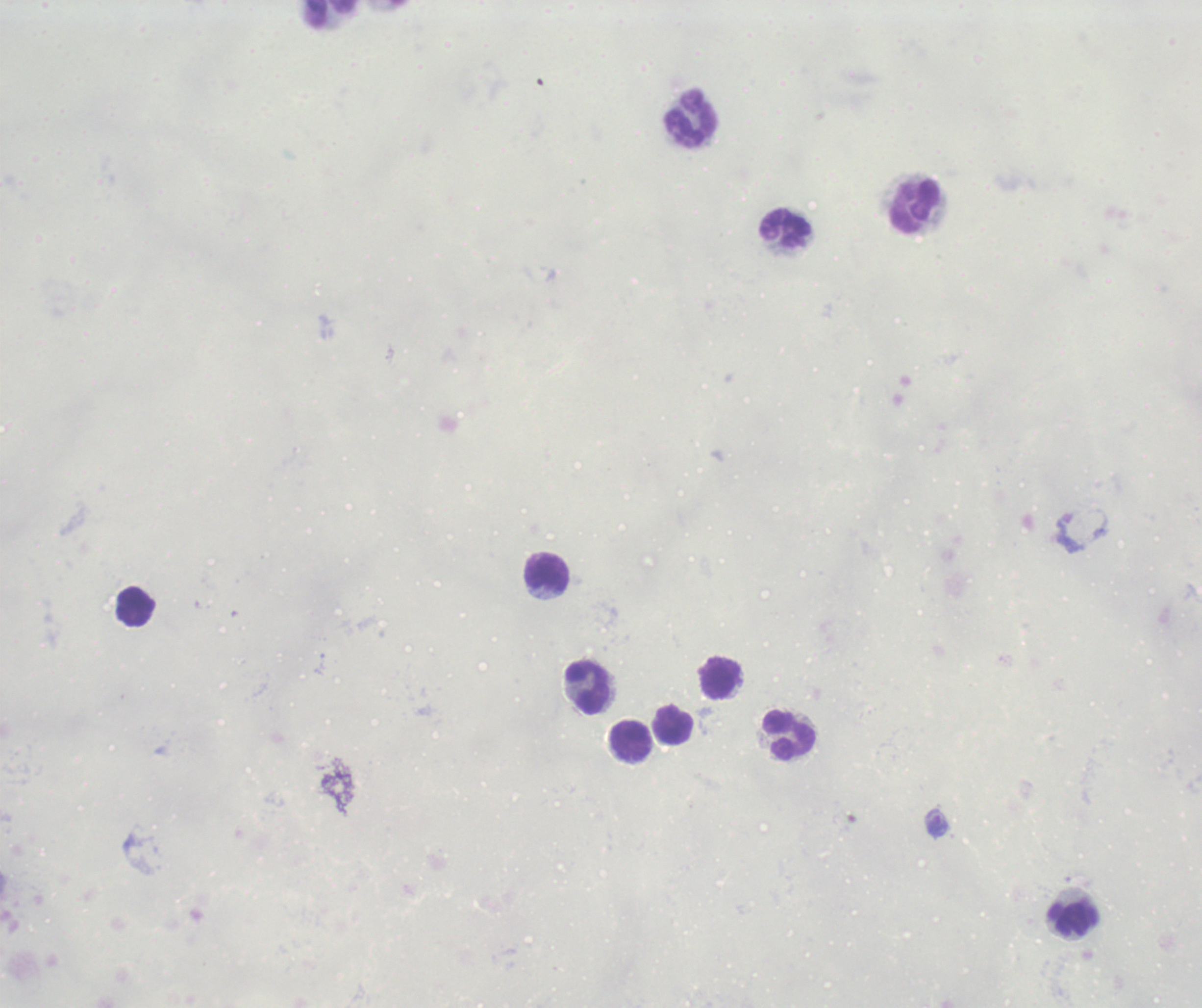
Approximate object centers, in pixels from the top-left corner. Leukocyte locations: (x=332, y=14), (x=692, y=119), (x=916, y=206), (x=786, y=228), (x=547, y=573), (x=137, y=607), (x=719, y=679), (x=590, y=689), (x=672, y=727), (x=790, y=734), (x=631, y=741), (x=1073, y=919). Trophozoite locations: (x=937, y=824). Image is 1202×1008 pixels. Thick blood smear. One field from this slide. Background quality: poor. Result: positive for Plasmodium parasites. Captured at 100x magnification. Romanowsky stain. Previously used in a real diagnosis.